Classify this cell by malaria status.
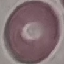

It is uninfected.

Summary:
  - Preparation: thin blood film
  - Stain: Giemsa
  - Capture: smartphone camera at the microscope eyepiece
  - Image type: automatically extracted cell patch, resized to 64 × 64 pixels